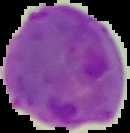
image type = segmented cell region with the area outside set to black
malaria status = parasitized
image size = 130×133 pixels
preparation = thin blood smear